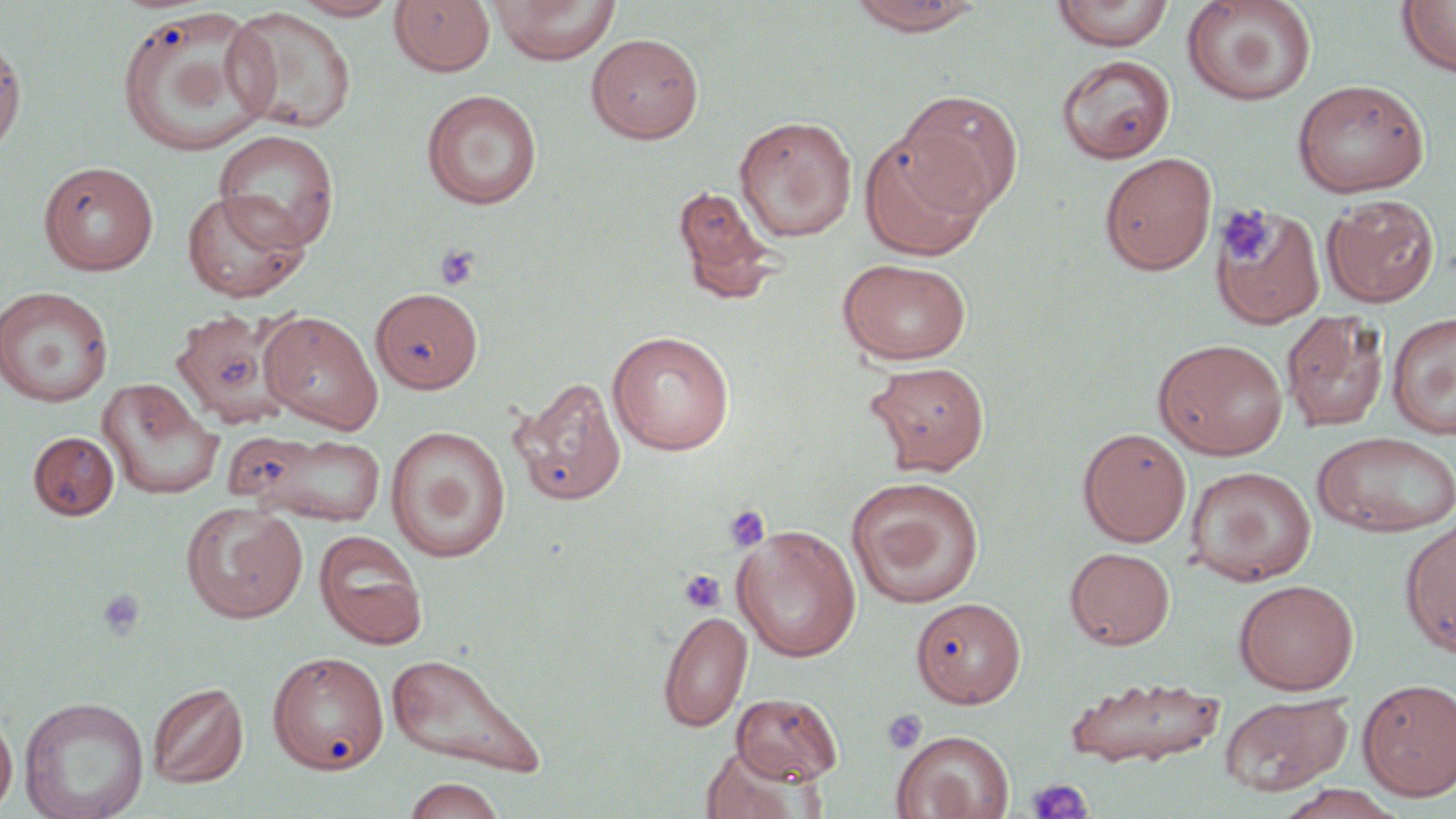
slide-level diagnosis = no evidence of blood parasites
preparation = thin blood film
magnification = 1000x
image size = 1456×819 pixels
platelet locations = approximate bounding boxes as [x1, y1, x2, y2] in pixels: [1217, 206, 1275, 265], [434, 243, 480, 290], [723, 504, 771, 553], [678, 569, 727, 614], [97, 588, 145, 640], [882, 709, 927, 754], [1026, 777, 1092, 819]
stain = May-Grünwald-Giemsa
uninfected red blood cell locations = approximate bounding boxes as [x1, y1, x2, y2] in pixels: [289, 0, 400, 20], [389, 0, 495, 78], [489, 0, 621, 65], [844, 0, 989, 36], [1051, 0, 1174, 52], [1181, 0, 1318, 107], [1397, 0, 1456, 78], [115, 7, 273, 155], [224, 7, 357, 135], [586, 32, 704, 144], [0, 33, 27, 161], [1057, 55, 1175, 163], [1292, 78, 1429, 197], [422, 89, 542, 210], [893, 89, 1023, 218], [733, 115, 857, 242], [214, 129, 340, 252], [858, 133, 987, 262], [1099, 152, 1217, 274], [37, 160, 160, 275], [671, 184, 781, 304], [181, 190, 308, 302], [1322, 194, 1440, 307], [1212, 205, 1325, 327], [837, 258, 972, 365], [0, 286, 114, 408], [370, 287, 482, 394], [169, 308, 306, 429], [1280, 309, 1390, 433], [1387, 311, 1456, 439], [261, 312, 383, 434], [607, 331, 735, 455], [1153, 338, 1288, 460], [864, 361, 990, 476], [509, 376, 627, 507], [96, 378, 225, 500], [385, 425, 511, 563], [1077, 427, 1192, 546], [228, 430, 387, 525], [28, 431, 119, 520], [1311, 431, 1456, 538], [1185, 465, 1317, 586], [844, 476, 985, 609], [181, 501, 308, 624], [1399, 517, 1456, 657], [731, 524, 861, 662], [313, 530, 428, 649], [1065, 546, 1175, 649], [1233, 579, 1359, 694], [911, 597, 1026, 708], [658, 610, 753, 732], [267, 651, 389, 774], [385, 651, 548, 777], [1062, 674, 1225, 768], [1358, 678, 1456, 801], [147, 682, 248, 788], [731, 693, 844, 784], [1219, 693, 1354, 797], [18, 695, 149, 819], [0, 708, 17, 816], [891, 730, 1015, 818], [701, 745, 815, 819], [402, 776, 507, 819], [1274, 784, 1406, 819]
field of view = one of a larger specimen
modality = optical microscopy